Classify this cell by malaria status.
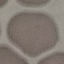
It is uninfected.

image type = automatically extracted cell patch, resized to 64 × 64 pixels
capture = smartphone camera at the microscope eyepiece
preparation = thin blood smear
stain = Giemsa